Classify this cell by malaria status.
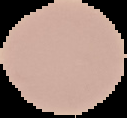

Uninfected.

Segmented cell region on a black background. Image is 127×118 pixels. From a thin blood smear.